Find each white blood cell.
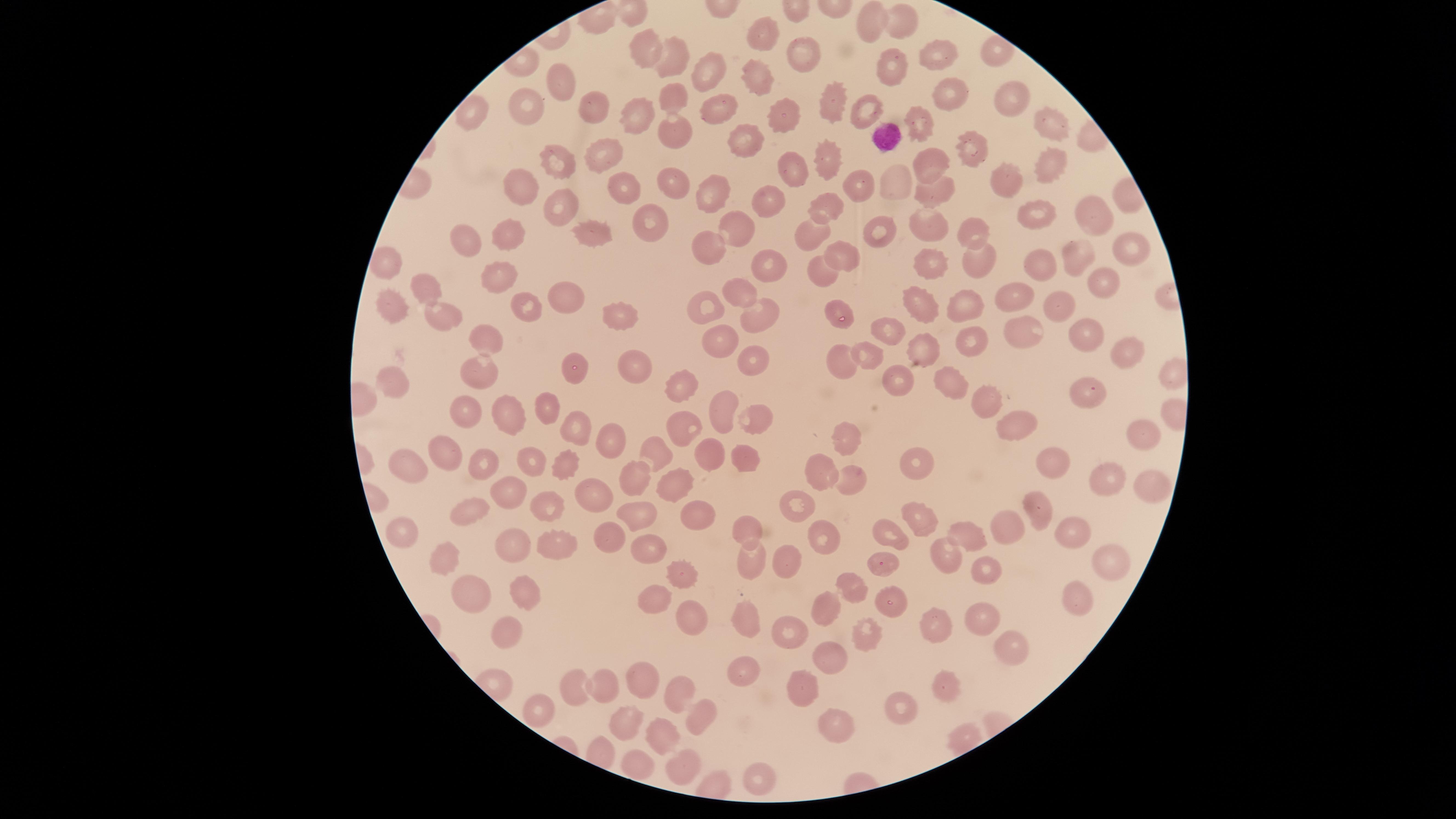

No white blood cells identified.

Approximate marker points as [x, y] in pixels.
Summary:
  - Uninfected red blood cells: [877, 21], [896, 21], [767, 32], [799, 51], [934, 54], [653, 55], [679, 62], [894, 68], [713, 71], [558, 79], [754, 81], [831, 95], [949, 95], [669, 96], [1008, 102], [527, 107], [589, 107], [470, 110], [716, 110], [862, 112], [635, 113], [781, 114], [917, 119], [1046, 122], [671, 131], [748, 140], [974, 149], [601, 154], [559, 162], [927, 162], [1053, 162], [824, 163], [791, 168], [1007, 180], [527, 182], [892, 182], [675, 183], [622, 186], [863, 188], [707, 192], [935, 192], [766, 202], [823, 206], [564, 207], [1035, 213], [1088, 216], [653, 227], [736, 228], [930, 228], [966, 228], [584, 233], [886, 233], [813, 235], [470, 236], [513, 236], [706, 246], [1130, 246], [841, 250], [1080, 257], [766, 260], [933, 260], [973, 260], [1045, 263], [380, 267], [823, 269], [493, 277], [1099, 280], [430, 286], [738, 290], [552, 293], [1009, 299], [706, 303], [965, 303], [926, 305], [1060, 305], [393, 307], [837, 307], [528, 308], [623, 313], [755, 313], [451, 318], [1019, 330], [886, 332], [1085, 333], [965, 338], [483, 340], [726, 342], [920, 346], [1125, 352], [874, 356], [840, 357], [754, 360], [632, 365], [575, 368], [476, 370], [897, 375], [946, 381], [393, 383], [682, 388], [1090, 396], [719, 404], [545, 405], [986, 406], [461, 407], [750, 419], [511, 420], [577, 423], [678, 430], [1017, 430], [1142, 433], [844, 440], [613, 443], [442, 448], [706, 454], [656, 455], [533, 461], [911, 463], [408, 465], [748, 465], [1052, 465], [489, 468], [567, 469], [633, 470], [818, 475], [1101, 476], [680, 482], [1145, 485], [846, 487], [505, 493], [593, 493], [549, 508], [799, 508], [1038, 513], [474, 514], [635, 515], [701, 518], [917, 520], [747, 528], [1007, 529], [405, 530], [970, 534], [1071, 534], [603, 535], [898, 538], [821, 540], [650, 542], [562, 549], [513, 551], [435, 554], [748, 555], [945, 555], [1109, 558], [885, 560], [788, 563], [989, 570], [679, 571], [853, 588], [473, 591], [1075, 594], [525, 595], [650, 601], [888, 603], [832, 606], [979, 618], [696, 619], [743, 619], [934, 625], [501, 627], [790, 627], [865, 632], [1008, 648], [831, 656], [737, 663], [646, 677], [949, 683], [572, 684], [601, 685], [806, 691], [679, 695], [898, 705], [533, 713], [699, 717], [625, 721], [828, 725], [665, 741], [635, 763], [680, 769], [748, 780]
  - Visible region: circular
  - Field of view: single
  - Image size: 1456×819 pixels
  - Preparation: thin blood smear
  - Stain: Giemsa
  - Capture: smartphone photograph through the microscope eyepiece
  - Presence: no malaria parasites identified